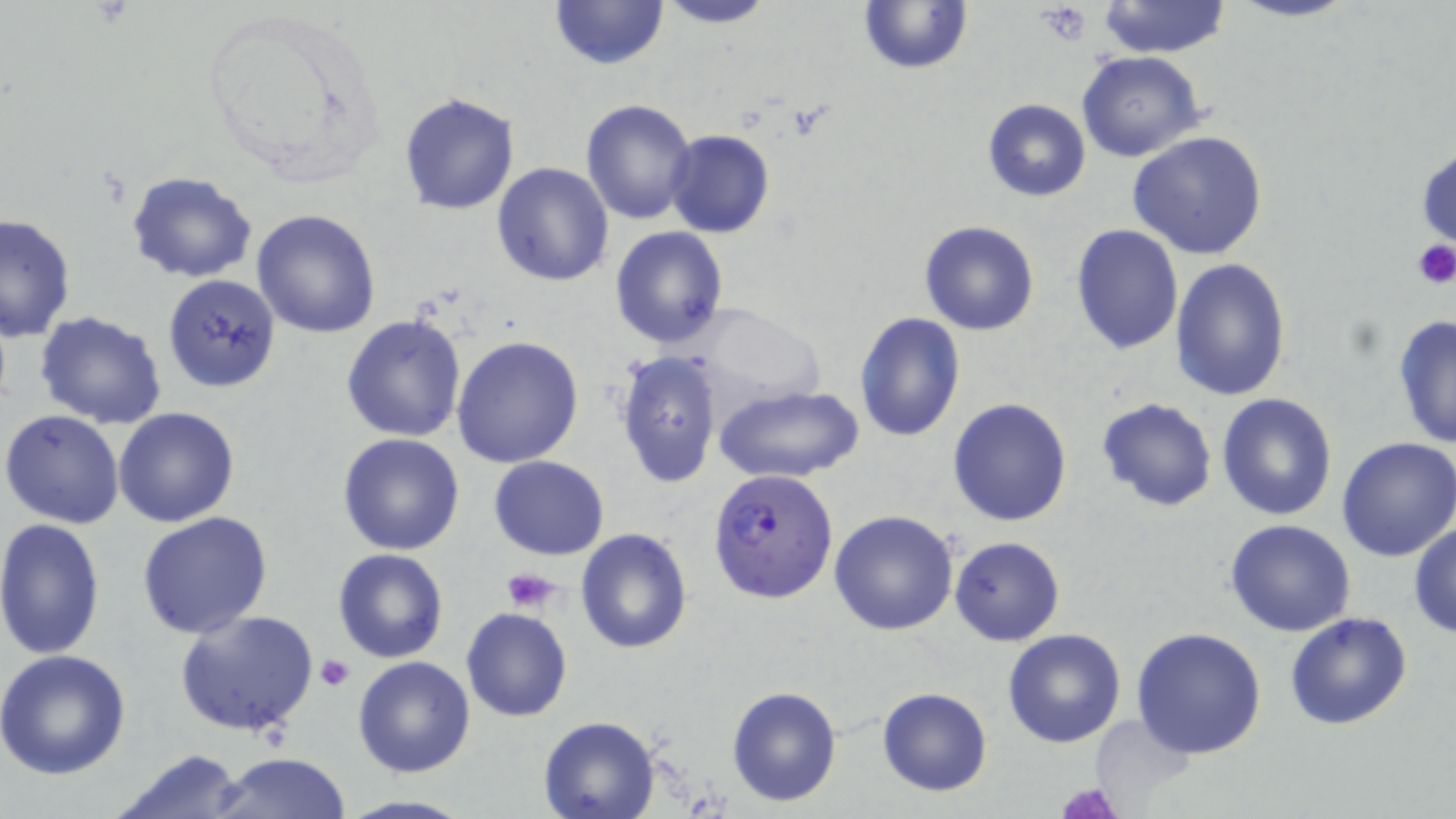

Approximate bounding boxes as named x1/y1/x2/y2 corners in pixels. Plasmodium falciparum-infected red blood cell locations: (x1=707, y1=469, x2=839, y2=603). Uninfected red blood cell locations: (x1=549, y1=0, x2=669, y2=71), (x1=653, y1=0, x2=779, y2=28), (x1=1228, y1=0, x2=1360, y2=23), (x1=857, y1=1, x2=973, y2=76), (x1=1096, y1=1, x2=1232, y2=58), (x1=1077, y1=50, x2=1205, y2=161), (x1=398, y1=93, x2=520, y2=215), (x1=580, y1=98, x2=700, y2=225), (x1=981, y1=98, x2=1092, y2=201), (x1=664, y1=129, x2=774, y2=239), (x1=1128, y1=130, x2=1269, y2=261), (x1=1415, y1=143, x2=1455, y2=255), (x1=492, y1=163, x2=615, y2=285), (x1=125, y1=172, x2=258, y2=282), (x1=252, y1=208, x2=383, y2=339), (x1=1, y1=212, x2=75, y2=340), (x1=919, y1=221, x2=1039, y2=335), (x1=1071, y1=223, x2=1182, y2=356), (x1=610, y1=226, x2=728, y2=350), (x1=1170, y1=257, x2=1291, y2=401), (x1=163, y1=273, x2=281, y2=393), (x1=688, y1=306, x2=828, y2=409), (x1=33, y1=311, x2=166, y2=428), (x1=855, y1=311, x2=964, y2=441), (x1=341, y1=314, x2=468, y2=442), (x1=1392, y1=314, x2=1456, y2=450), (x1=452, y1=336, x2=585, y2=468), (x1=614, y1=351, x2=723, y2=488), (x1=713, y1=385, x2=862, y2=485), (x1=1218, y1=393, x2=1337, y2=521), (x1=948, y1=397, x2=1073, y2=526), (x1=1096, y1=398, x2=1218, y2=513), (x1=114, y1=408, x2=240, y2=527), (x1=2, y1=409, x2=126, y2=529), (x1=337, y1=433, x2=465, y2=555), (x1=1336, y1=436, x2=1456, y2=561), (x1=489, y1=456, x2=609, y2=559), (x1=829, y1=509, x2=959, y2=636), (x1=137, y1=512, x2=273, y2=641), (x1=0, y1=518, x2=105, y2=660), (x1=1226, y1=520, x2=1356, y2=637), (x1=1409, y1=521, x2=1456, y2=637), (x1=576, y1=529, x2=692, y2=652), (x1=949, y1=535, x2=1065, y2=645), (x1=333, y1=548, x2=449, y2=663), (x1=461, y1=608, x2=572, y2=723), (x1=176, y1=609, x2=318, y2=738), (x1=1285, y1=611, x2=1414, y2=731), (x1=1132, y1=628, x2=1267, y2=759), (x1=1003, y1=629, x2=1126, y2=747), (x1=0, y1=648, x2=131, y2=778), (x1=352, y1=655, x2=476, y2=776), (x1=726, y1=684, x2=844, y2=807), (x1=876, y1=686, x2=991, y2=797), (x1=1089, y1=713, x2=1197, y2=809), (x1=538, y1=716, x2=658, y2=819), (x1=109, y1=750, x2=252, y2=818), (x1=208, y1=752, x2=355, y2=819), (x1=334, y1=794, x2=477, y2=819). Platelet locations: (x1=1037, y1=4, x2=1093, y2=44), (x1=1410, y1=238, x2=1456, y2=289), (x1=503, y1=566, x2=562, y2=614), (x1=314, y1=654, x2=354, y2=693), (x1=1055, y1=783, x2=1122, y2=819). Slide-level diagnosis: Plasmodium falciparum. 1000x magnification. Thin blood smear. May-Grünwald-Giemsa-stained preparation. Light microscopy. Image is 1456×819 pixels. Single field of view.